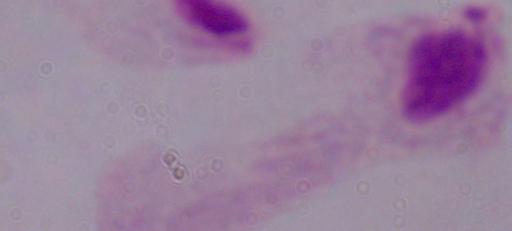
Summary:
  - Magnification: 1000x
  - Identification: trichomonad
  - Modality: micrograph